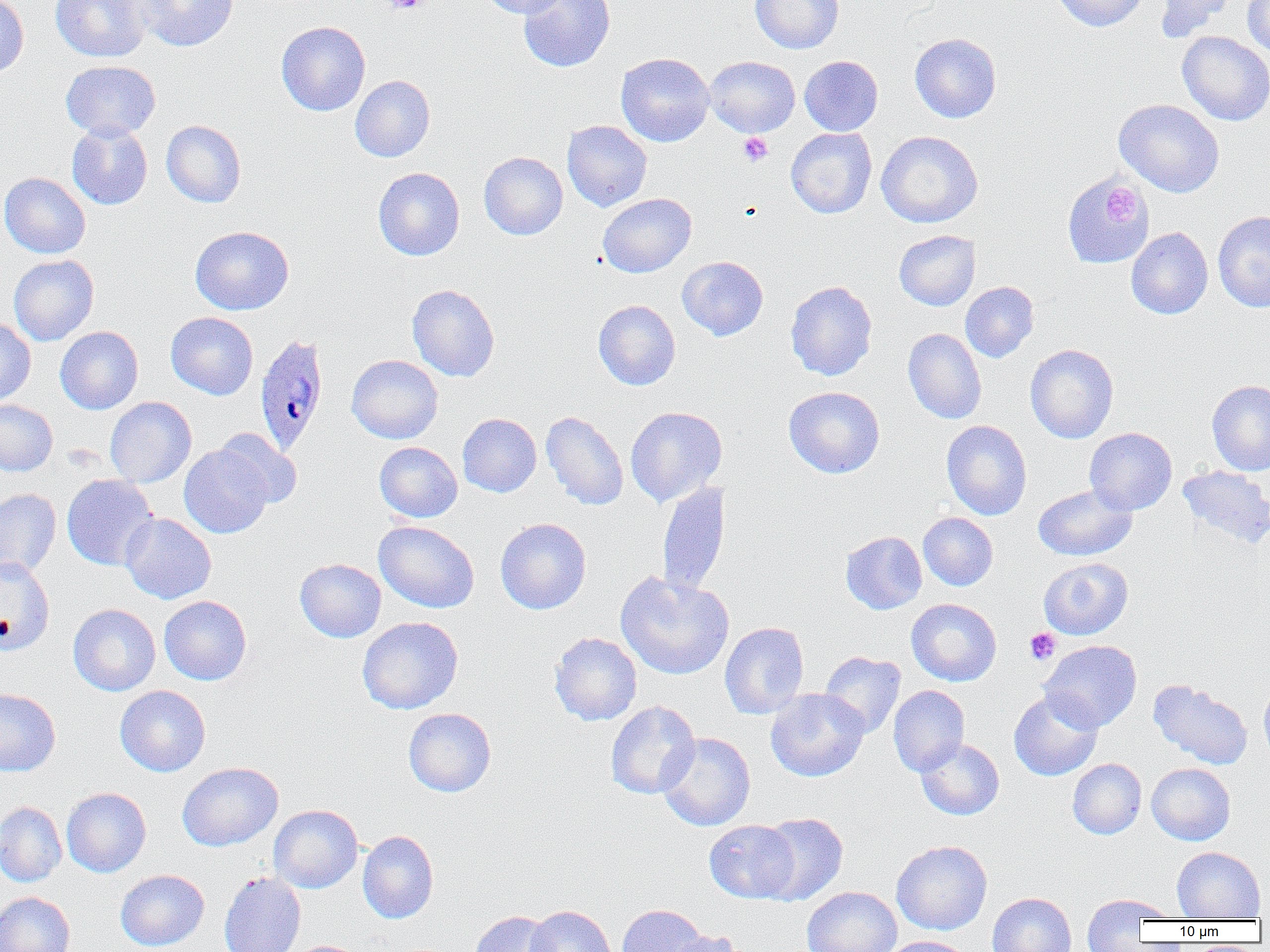
Approximate bounding boxes as (x1, y1, x2, y2) in pixels. Platelet locations: (383, 0, 430, 14), (738, 132, 773, 166), (1103, 185, 1140, 223), (1025, 628, 1061, 664). Uninfected red blood cell locations: (0, 0, 29, 78), (50, 0, 152, 62), (136, 0, 238, 51), (479, 0, 569, 18), (518, 0, 615, 72), (750, 0, 844, 53), (1051, 0, 1149, 31), (1154, 0, 1235, 41), (1242, 1, 1270, 57), (276, 21, 370, 116), (1177, 31, 1270, 125), (909, 33, 1001, 123), (615, 52, 715, 147), (799, 55, 883, 136), (705, 56, 800, 137), (61, 60, 160, 140), (350, 75, 435, 162), (1114, 99, 1225, 197), (161, 120, 246, 208), (562, 120, 652, 212), (66, 122, 153, 210), (786, 128, 877, 218), (876, 130, 983, 228), (479, 152, 568, 240), (373, 167, 465, 260), (0, 173, 90, 258), (1063, 175, 1153, 271), (598, 193, 696, 278), (1213, 210, 1270, 312), (190, 225, 294, 315), (1126, 227, 1213, 319), (894, 230, 980, 310), (8, 255, 99, 345), (677, 256, 768, 340), (785, 280, 877, 381), (960, 281, 1039, 362), (407, 284, 500, 381), (593, 300, 680, 390), (165, 312, 258, 400), (0, 318, 35, 405), (55, 326, 143, 414), (903, 328, 987, 424), (1025, 344, 1119, 443), (346, 355, 443, 443), (1207, 380, 1270, 475), (783, 386, 884, 478), (105, 397, 196, 487), (0, 400, 57, 476), (625, 406, 727, 507), (541, 411, 629, 510), (457, 413, 542, 497), (941, 420, 1032, 520), (1084, 427, 1177, 515), (213, 429, 302, 508), (374, 442, 462, 522), (179, 445, 274, 538), (1177, 465, 1270, 548), (61, 474, 158, 570), (656, 481, 730, 599), (1033, 484, 1137, 561), (0, 488, 61, 579), (120, 512, 216, 604), (918, 512, 998, 591), (495, 517, 591, 614), (374, 521, 479, 613), (840, 531, 927, 614), (0, 557, 55, 656), (1038, 557, 1133, 639), (295, 558, 386, 642), (614, 570, 734, 680), (159, 595, 252, 685), (906, 598, 1002, 686), (68, 604, 160, 696), (357, 616, 463, 714), (720, 621, 809, 719), (549, 632, 642, 726), (1039, 640, 1142, 732), (819, 651, 905, 737), (1259, 677, 1270, 764), (1149, 679, 1253, 770), (115, 685, 210, 776), (888, 685, 969, 776), (0, 688, 61, 776), (765, 688, 869, 782), (1009, 689, 1104, 781), (605, 700, 700, 799), (403, 707, 496, 797), (656, 732, 755, 831), (915, 738, 1004, 820), (1067, 758, 1146, 839), (177, 762, 283, 851), (1146, 763, 1235, 845), (61, 787, 151, 877), (0, 801, 67, 887), (268, 804, 362, 893), (755, 812, 848, 905), (704, 820, 799, 903), (358, 830, 438, 923), (891, 840, 992, 935), (1172, 846, 1265, 920), (115, 869, 209, 951), (219, 872, 306, 952), (802, 886, 902, 951), (0, 892, 76, 952), (987, 892, 1076, 952), (1081, 894, 1167, 951), (1090, 895, 1177, 922), (617, 904, 709, 952), (526, 905, 616, 952), (470, 910, 559, 952), (663, 930, 746, 952), (880, 936, 972, 952). Plasmodium ovale-infected red blood cell locations: (254, 333, 330, 455). Slide-level diagnosis: Plasmodium ovale. Thin blood film. Light microscopy. 1000x magnification. One field of a larger specimen. Image is 1270×952 pixels.